State which cell type is depicted.
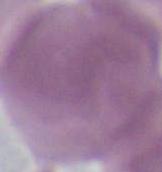

An erythrocyte.

magnification: 1000x
modality: micrograph